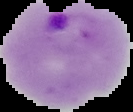

{
  "preparation": "thin blood film",
  "malaria_status": "parasitized",
  "image_type": "segmented cell region on a black background",
  "image_size": "133×112 pixels"
}